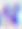

Summary:
  - Identification: Toxoplasma gondii
  - Modality: micrograph
  - Magnification: 400x